Outline platelets.
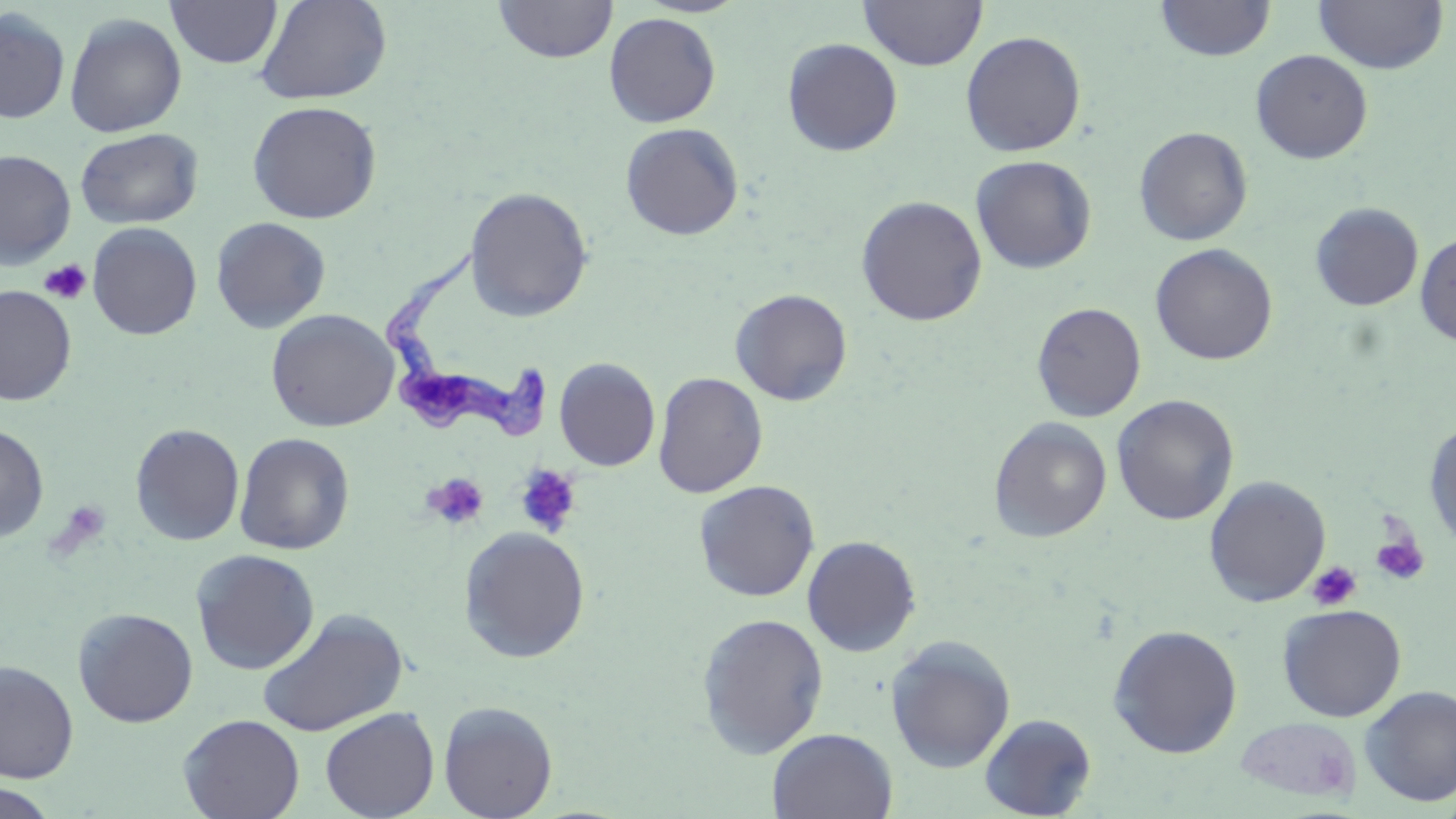

Approximate bounding boxes as (x1, y1, x2, y2) in pixels.
Platelets: (39, 259, 92, 305), (515, 465, 582, 537), (423, 472, 489, 530), (1370, 524, 1430, 588), (1306, 560, 1361, 612).

Summary:
  - Trypanosoma brucei locations: (377, 244, 551, 445)
  - Uninfected red blood cell locations: (255, 0, 393, 105), (493, 0, 618, 63), (858, 0, 988, 71), (1156, 0, 1276, 61), (166, 1, 282, 69), (1313, 1, 1449, 74), (0, 8, 71, 125), (64, 12, 187, 138), (604, 12, 721, 127), (960, 30, 1086, 157), (782, 38, 903, 157), (1251, 49, 1373, 163), (246, 100, 382, 224), (620, 123, 744, 241), (1134, 126, 1253, 246), (75, 127, 203, 229), (0, 149, 76, 268), (970, 155, 1096, 274), (463, 186, 594, 322), (856, 195, 988, 326), (1310, 202, 1424, 311), (210, 217, 331, 334), (87, 222, 202, 340), (1414, 230, 1456, 346), (1150, 243, 1278, 366), (1, 285, 76, 406), (730, 288, 853, 406), (1032, 302, 1146, 422), (265, 308, 399, 432), (554, 357, 660, 471), (652, 372, 768, 498), (1112, 395, 1239, 526), (988, 417, 1112, 542), (1424, 418, 1456, 551), (0, 423, 50, 543), (130, 423, 245, 546), (234, 432, 355, 554), (1204, 475, 1331, 606), (693, 479, 820, 602), (458, 526, 591, 663), (802, 535, 922, 657), (190, 549, 320, 675), (1277, 603, 1407, 722), (72, 607, 198, 727), (257, 608, 408, 737), (695, 612, 830, 758), (1107, 624, 1243, 758), (884, 635, 1016, 774), (0, 661, 79, 783), (1359, 684, 1456, 807), (438, 700, 558, 819), (320, 707, 439, 819), (178, 713, 304, 819), (979, 713, 1097, 818), (1235, 716, 1363, 803), (767, 727, 898, 819), (0, 782, 61, 819)
  - Slide-level diagnosis: Trypanosoma brucei
  - Modality: light microscopy
  - Stain: May-Grünwald-Giemsa
  - Magnification: 1000x
  - Preparation: thin blood film
  - Field of view: one of a larger specimen
  - Image size: 1456×819 pixels